Name the parasite shown.
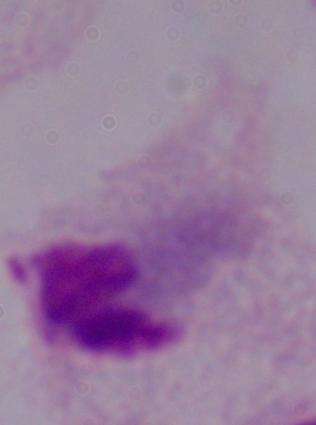
This is a trichomonad.

Micrograph. 1000x magnification.